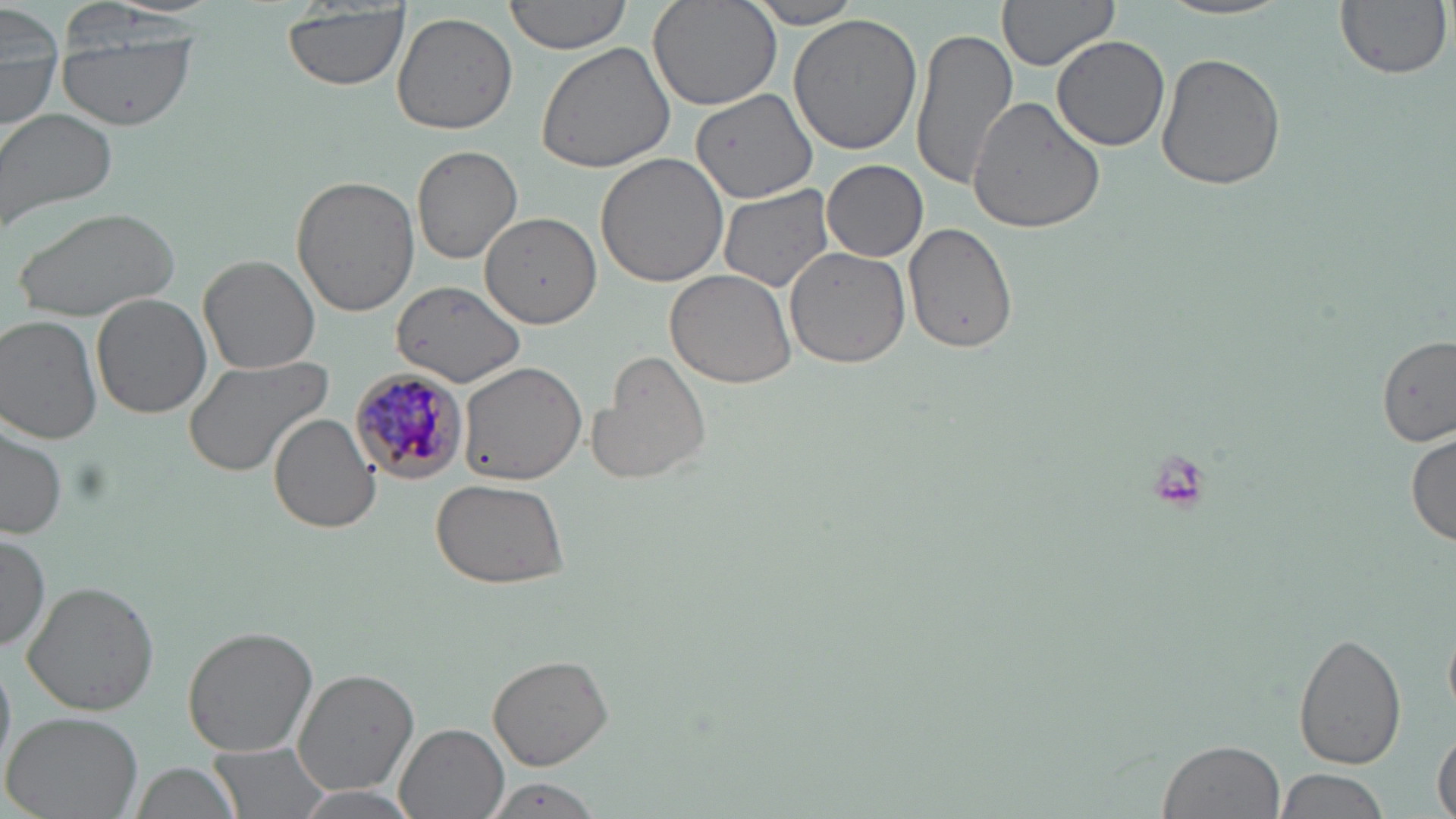

slide-level diagnosis = Plasmodium malariae
modality = optical microscopy
magnification = 1000x
image size = 1456×819 pixels
stain = May-Grünwald-Giemsa
uninfected red blood cell locations = approximate bounding boxes as (x1,y1)-(x2,y2) corner pairs in pixels: (505,0)-(636,55), (646,0)-(782,113), (996,0)-(1119,72), (1156,0)-(1296,21), (1334,0)-(1451,79), (743,1)-(869,28), (2,3)-(64,134), (281,6)-(410,89), (57,7)-(197,131), (392,11)-(518,136), (788,13)-(923,157), (910,25)-(1018,191), (1051,34)-(1171,151), (537,40)-(679,175), (1156,52)-(1287,191), (691,87)-(817,205), (967,96)-(1104,235), (0,107)-(119,236), (410,144)-(522,264), (595,152)-(732,289), (822,159)-(928,263), (291,175)-(418,317), (716,185)-(835,294), (14,205)-(182,321), (480,211)-(601,329), (903,224)-(1019,355), (784,248)-(910,369), (200,253)-(322,374), (665,269)-(798,388), (393,280)-(527,387), (92,293)-(212,421), (2,315)-(101,445), (1375,334)-(1456,443), (583,350)-(713,486), (181,354)-(334,479), (457,362)-(587,481), (213,377)-(361,520), (268,413)-(381,534), (0,420)-(66,539), (1408,430)-(1455,548), (430,477)-(574,586), (0,529)-(50,653), (23,580)-(159,717), (181,625)-(319,757), (1292,631)-(1409,774), (486,653)-(614,770), (292,667)-(418,794), (3,710)-(146,818), (395,723)-(509,819), (1432,732)-(1455,819), (1158,737)-(1284,818), (207,740)-(331,819), (127,760)-(246,819), (1274,767)-(1387,819), (483,778)-(602,818), (284,787)-(427,819)
field of view = one of a larger specimen
Plasmodium malariae-infected red blood cell locations = approximate bounding boxes as (x1,y1)-(x2,y2) corner pairs in pixels: (349,367)-(468,485)
preparation = thin blood film